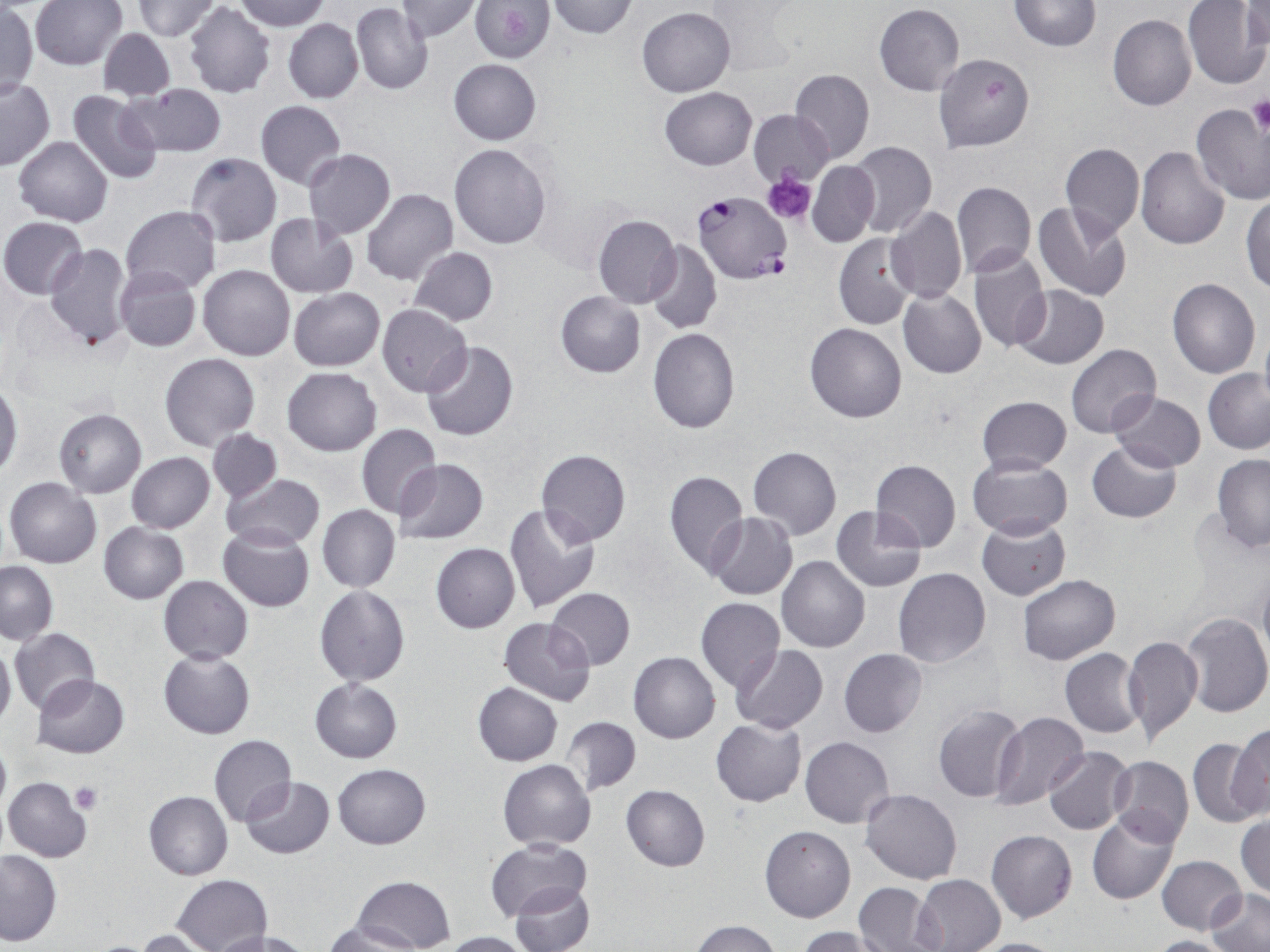 Approximate bounding boxes as (x1, y1, x2, y2) in pixels. Plasmodium falciparum-infected red blood cell locations: (694, 192, 791, 284). Platelet locations: (500, 10, 530, 39), (1248, 95, 1270, 136), (764, 171, 817, 225), (70, 782, 103, 813). Uninfected red blood cell locations: (234, 0, 330, 31), (469, 0, 556, 63), (1010, 0, 1101, 51), (30, 1, 128, 70), (131, 1, 221, 41), (396, 1, 482, 41), (546, 1, 639, 39), (1183, 1, 1269, 89), (1244, 1, 1270, 52), (874, 3, 965, 95), (1, 4, 38, 99), (183, 4, 275, 98), (351, 4, 433, 95), (637, 7, 736, 97), (1108, 13, 1196, 110), (283, 17, 363, 103), (96, 27, 178, 101), (932, 52, 1035, 154), (448, 58, 542, 145), (789, 69, 874, 163), (0, 79, 55, 170), (123, 84, 228, 159), (660, 87, 757, 170), (66, 89, 164, 185), (256, 100, 345, 188), (1190, 104, 1270, 204), (749, 109, 832, 186), (14, 136, 112, 225), (848, 142, 936, 237), (863, 143, 951, 303), (1060, 143, 1144, 239), (449, 144, 551, 249), (1135, 146, 1230, 249), (303, 149, 395, 239), (185, 152, 280, 247), (807, 161, 879, 248), (951, 180, 1036, 278), (362, 188, 457, 284), (1242, 196, 1270, 292), (1033, 202, 1133, 302), (121, 205, 221, 293), (885, 206, 967, 305), (265, 213, 360, 298), (593, 214, 682, 308), (1, 216, 87, 299), (833, 233, 915, 330), (645, 238, 721, 335), (45, 243, 133, 353), (408, 246, 498, 325), (967, 247, 1051, 353), (198, 264, 295, 360), (114, 266, 201, 352), (1168, 278, 1261, 379), (1012, 285, 1108, 369), (897, 287, 986, 379), (288, 288, 385, 371), (556, 290, 646, 377), (376, 304, 472, 397), (804, 323, 906, 423), (1258, 325, 1270, 408), (647, 328, 740, 433), (422, 341, 519, 442), (1067, 344, 1161, 439), (160, 352, 260, 452), (282, 367, 382, 455), (1204, 367, 1270, 454), (1, 384, 21, 476), (1108, 391, 1206, 471), (973, 395, 1073, 475), (53, 408, 147, 498), (356, 423, 442, 520), (207, 428, 282, 503), (1086, 439, 1181, 523), (747, 445, 842, 541), (535, 449, 630, 546), (126, 452, 215, 533), (1212, 454, 1270, 550), (966, 455, 1074, 539), (392, 457, 488, 547), (870, 459, 962, 551), (664, 470, 747, 577), (222, 474, 325, 549), (4, 476, 101, 568), (317, 504, 401, 593), (502, 504, 600, 614), (831, 507, 926, 593), (707, 511, 797, 600), (976, 517, 1071, 600), (98, 522, 189, 604), (218, 525, 315, 612), (430, 543, 520, 632), (776, 556, 870, 654), (0, 560, 57, 644), (893, 567, 991, 668), (1257, 568, 1270, 670), (1018, 574, 1120, 663), (159, 575, 253, 664), (313, 586, 411, 688), (545, 587, 635, 670), (695, 596, 785, 691), (1181, 611, 1270, 718), (497, 616, 595, 706), (9, 627, 99, 714), (1122, 636, 1204, 747), (0, 641, 15, 728), (732, 645, 828, 734), (158, 648, 257, 739), (838, 648, 927, 737), (1059, 648, 1145, 737), (628, 651, 720, 743), (31, 675, 130, 758), (310, 678, 402, 763), (472, 683, 562, 765), (932, 704, 1028, 804), (991, 712, 1089, 810), (561, 716, 641, 796), (711, 718, 806, 806), (1228, 724, 1270, 821), (0, 735, 10, 820), (209, 735, 297, 827), (800, 736, 894, 828), (1186, 738, 1268, 829), (1045, 747, 1135, 834), (1108, 755, 1194, 846), (498, 760, 596, 849), (333, 763, 430, 848), (1105, 765, 1197, 925), (2, 776, 91, 862), (239, 777, 335, 860), (621, 784, 710, 872), (861, 789, 963, 884), (143, 792, 232, 880), (1087, 811, 1180, 906), (1236, 815, 1269, 898), (760, 825, 856, 923), (985, 830, 1078, 923), (483, 836, 592, 921), (0, 851, 62, 946), (1156, 855, 1248, 934), (172, 874, 271, 952), (914, 874, 1005, 950), (354, 875, 456, 952), (510, 882, 594, 952), (853, 882, 943, 952), (1206, 889, 1269, 952), (324, 919, 420, 951), (690, 920, 783, 952), (797, 926, 892, 952), (133, 928, 218, 952), (212, 929, 312, 952), (440, 930, 531, 952), (1148, 935, 1237, 952), (965, 937, 1065, 952). Slide-level diagnosis: Plasmodium falciparum. Image is 1270×952 pixels. Single field of view. 1000x magnification. Optical microscopy. Thin blood smear. May-Grünwald-Giemsa-stained preparation.